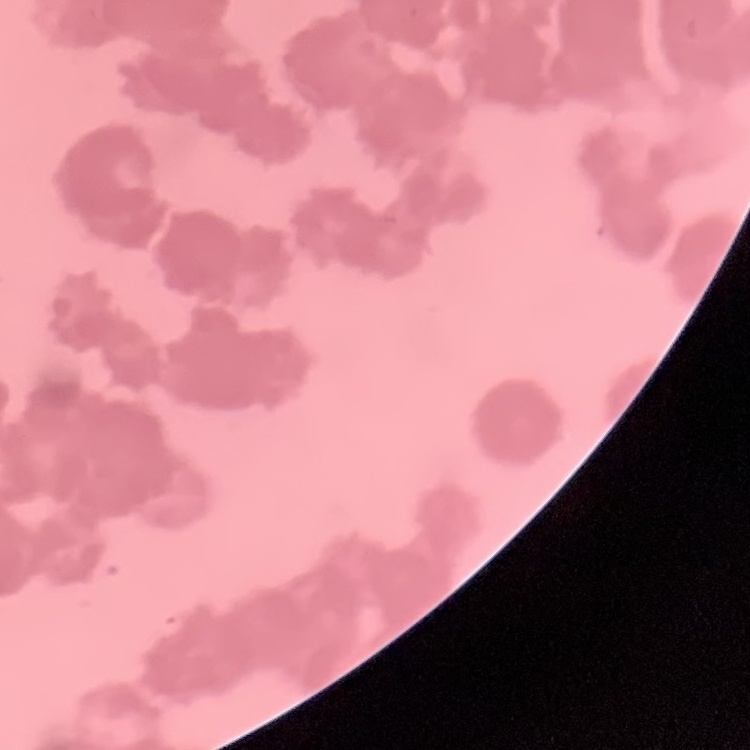
The red blood cells exhibit rouleaux formation. One tile cut from a larger photomicrograph. Stained with either Field's or Giemsa. Thin peripheral smear.